Classify this cell by malaria status.
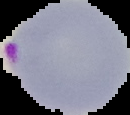

It is parasitized.

Image is 130×115 pixels. From a thin blood film. Cell region segmented out of the field of view; the surrounding area is masked to black.